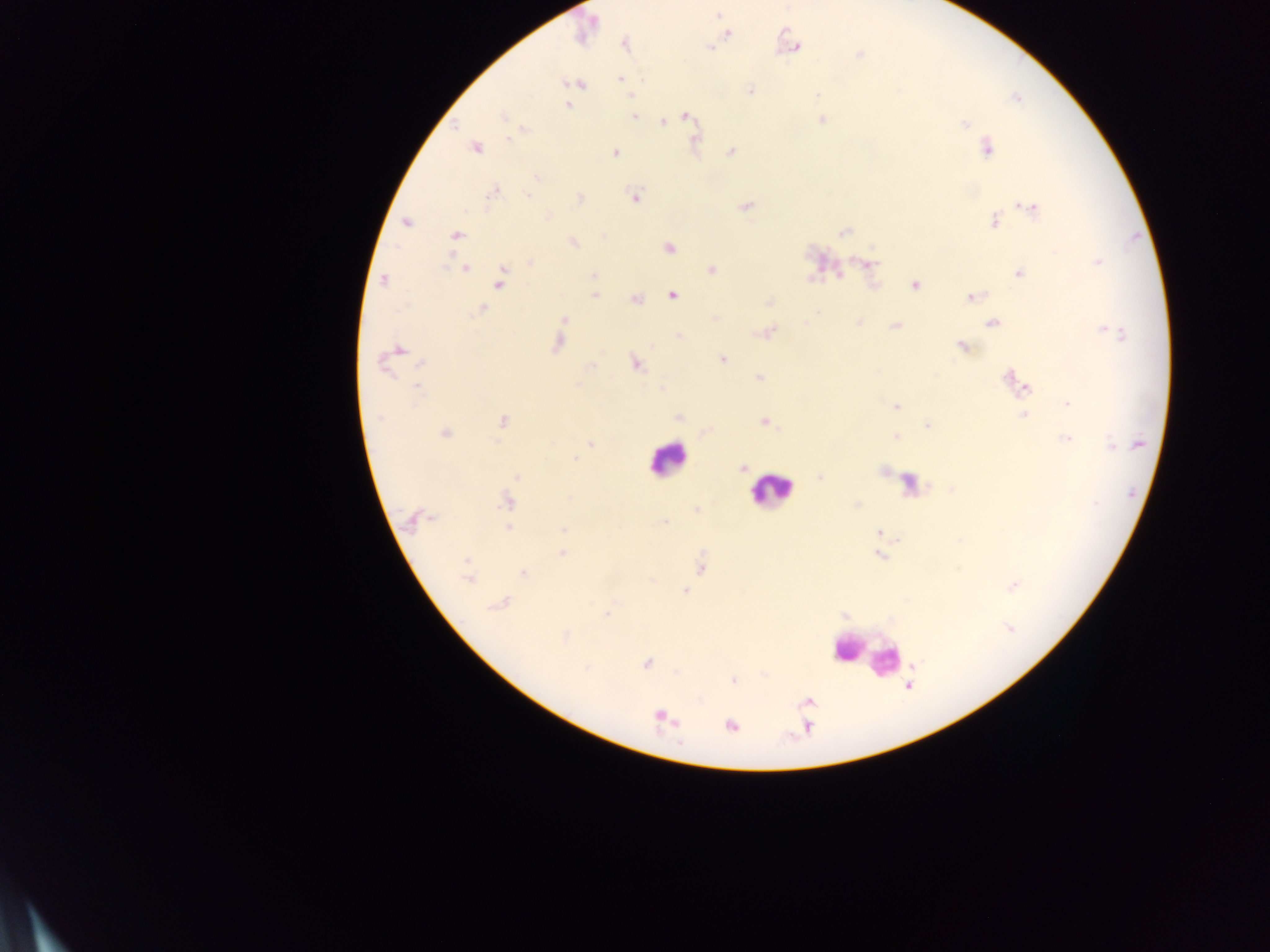

Approximate centers as {x, y} in pixels.
Summary:
  - Leukocyte locations: {667, 459}, {769, 490}, {846, 650}, {863, 654}
  - Plasmodium parasite locations: {718, 14}, {585, 28}, {728, 34}, {625, 44}, {795, 46}, {710, 48}, {859, 55}, {621, 79}, {642, 80}, {578, 84}, {750, 91}, {1017, 98}, {568, 106}, {502, 116}, {634, 117}, {686, 117}, {822, 120}, {662, 122}, {965, 124}, {525, 130}, {477, 147}, {987, 149}, {731, 152}, {615, 153}, {536, 178}, {492, 193}, {527, 195}, {635, 197}, {579, 198}, {745, 206}, {1030, 208}, {548, 216}, {994, 222}, {407, 223}, {845, 232}, {456, 235}, {574, 243}, {669, 248}, {530, 262}, {870, 263}, {1097, 263}, {464, 268}, {712, 269}, {1020, 273}, {593, 276}, {383, 280}, {499, 280}, {915, 286}, {672, 295}, {594, 296}, {973, 296}, {635, 299}, {769, 302}, {482, 309}, {818, 312}, {715, 318}, {564, 319}, {992, 324}, {894, 326}, {767, 333}, {1115, 333}, {678, 335}, {558, 343}, {962, 346}, {399, 349}, {723, 359}, {384, 364}, {423, 365}, {591, 365}, {636, 365}, {759, 377}, {1011, 379}, {1024, 386}, {418, 387}, {661, 390}, {1068, 404}, {896, 406}, {1024, 414}, {379, 417}, {678, 418}, {503, 421}, {764, 421}, {927, 425}, {445, 433}, {896, 437}, {1065, 439}, {590, 444}, {1137, 444}, {1112, 446}, {575, 458}, {742, 468}, {518, 477}, {821, 477}, {506, 502}, {857, 505}, {696, 510}, {413, 519}, {662, 522}, {508, 527}, {563, 530}, {879, 532}, {561, 554}, {879, 556}, {702, 569}, {524, 573}, {467, 577}, {1013, 586}, {685, 591}, {500, 603}, {607, 614}, {1009, 627}, {565, 636}, {646, 664}, {586, 668}, {733, 681}, {663, 717}, {731, 726}
  - Preparation: thick blood film
  - Capture: mobile-phone photograph through a microscope
  - Field of view: single
  - Country: Ghana
  - Image size: 1270×952 pixels